Report the malaria status of this cell.
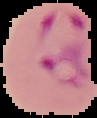
Parasitized.

Summary:
  - Preparation: thin blood smear
  - Image size: 97×118 pixels
  - Image type: segmented cell region on a black background